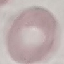

{
  "result": "no malaria parasites seen",
  "image_type": "cell patch, automatically extracted from a larger field of view and resized to 64 × 64 pixels",
  "stain": "Giemsa",
  "preparation": "thin blood film",
  "capture": "smartphone camera at the microscope eyepiece"
}